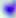
Summary:
  - Modality: photomicrograph
  - Identification: Toxoplasma gondii
  - Magnification: 400x